Identify the parasite.
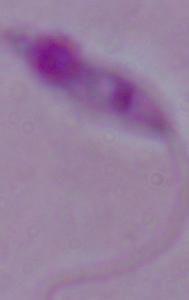

Leishmania.

Summary:
  - Modality: micrograph
  - Magnification: 1000x